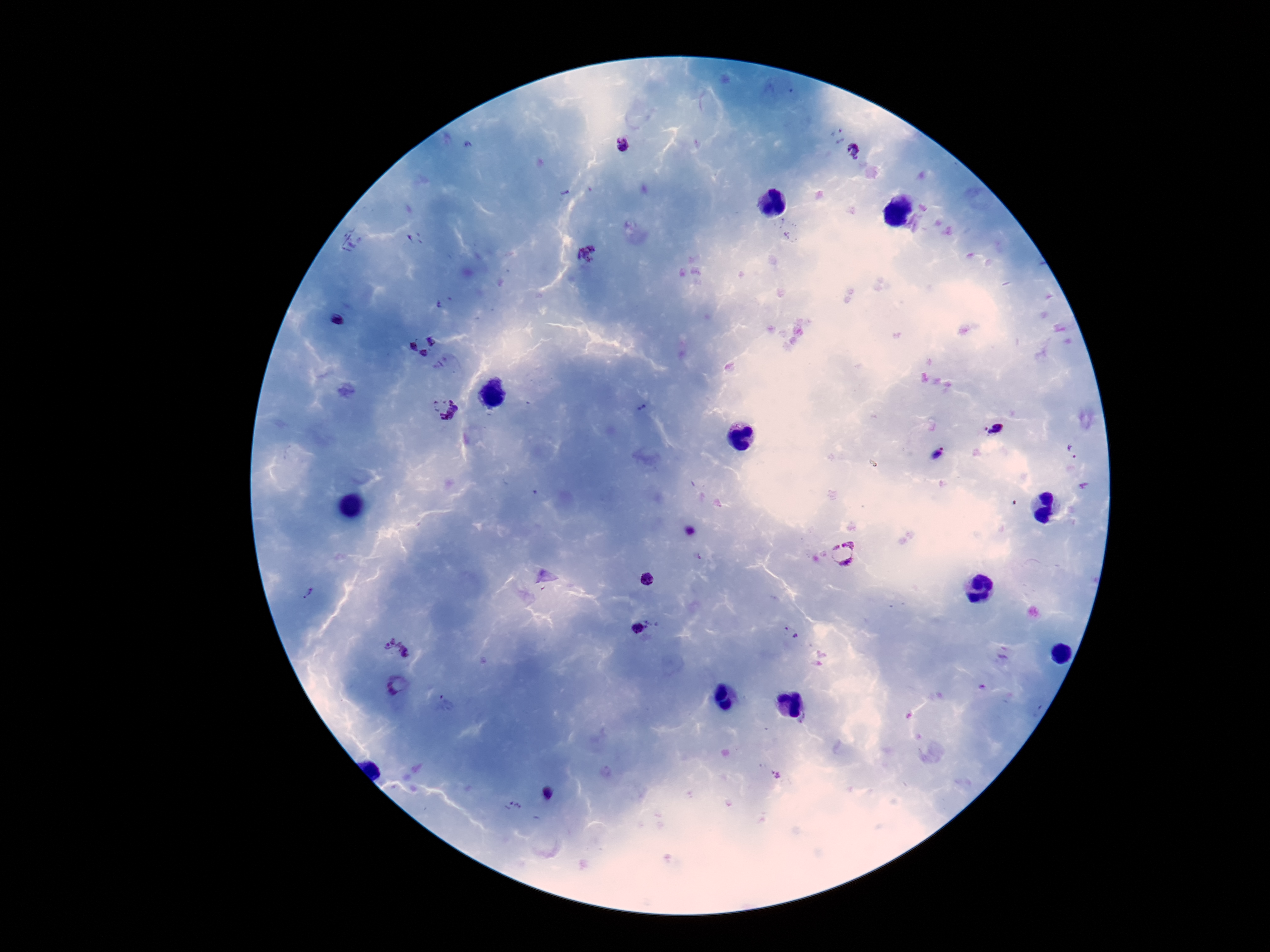

Approximate centers as {x, y} in pixels. Plasmodium parasite locations: {838, 136}, {625, 145}, {854, 152}, {587, 254}, {441, 305}, {337, 321}, {423, 344}, {445, 410}, {996, 429}, {939, 454}, {691, 532}, {842, 555}, {648, 580}, {307, 593}, {638, 627}, {790, 631}, {398, 649}, {398, 685}, {547, 793}, {514, 806}. 100x magnification. Giemsa stain. Thick blood smear. Patient malaria status: positive. Image is 1270×952 pixels. Smartphone photograph taken through the microscope eyepiece. One field from this slide.